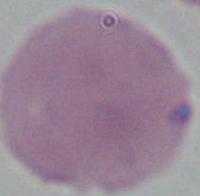
Summary:
  - Modality: micrograph
  - Magnification: 1000x
  - Identification: red blood cell